Outline each Plasmodium vivax-infected red blood cell.
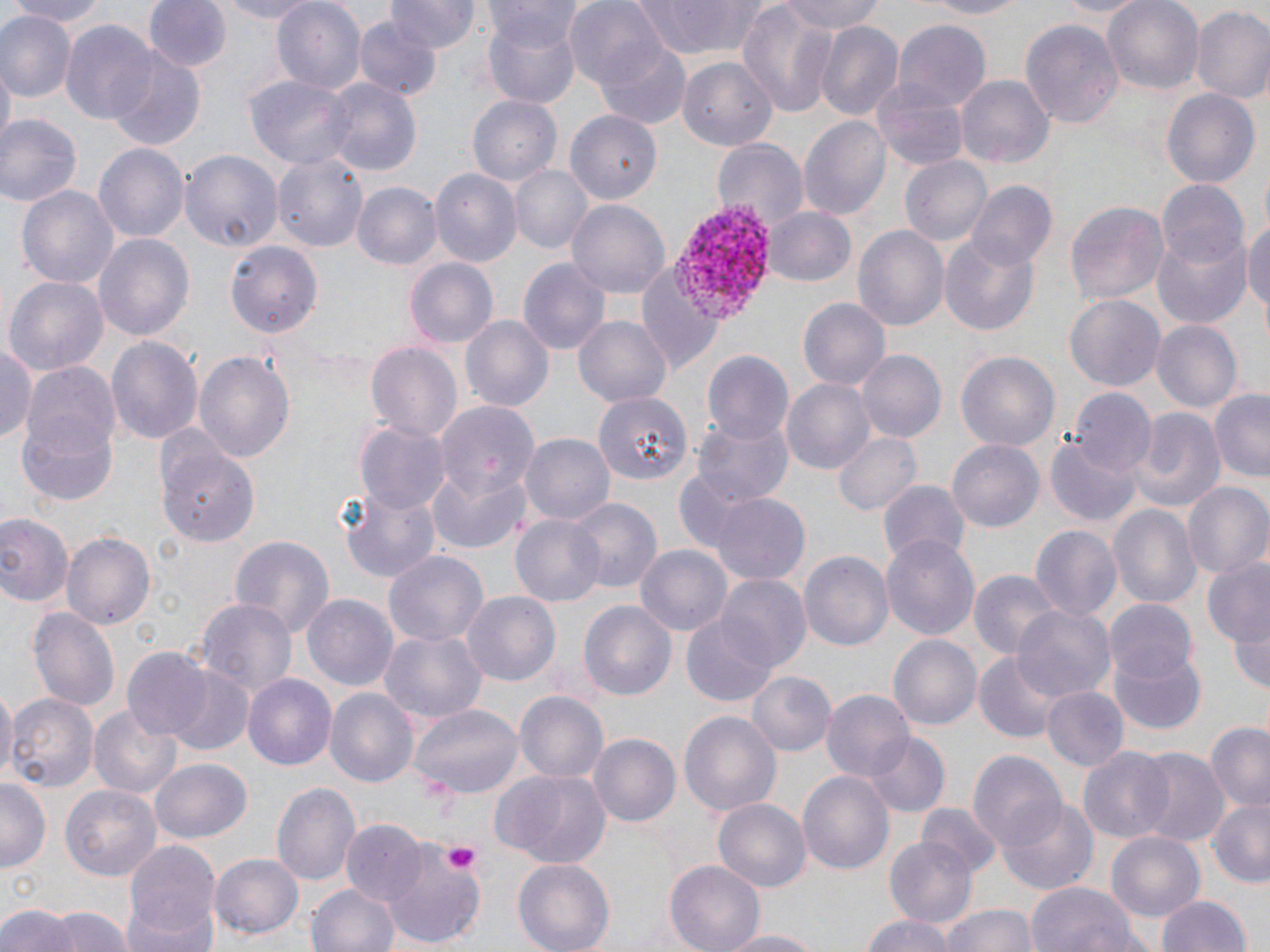
Approximate bounding boxes as named x1/y1/x2/y2 corners in pixels.
Plasmodium vivax-infected red blood cells: (x1=672, y1=202, x2=779, y2=319).

Platelet locations: (x1=445, y1=842, x2=480, y2=873). Uninfected red blood cell locations: (x1=1, y1=0, x2=112, y2=25), (x1=143, y1=0, x2=228, y2=73), (x1=204, y1=0, x2=325, y2=23), (x1=387, y1=0, x2=480, y2=54), (x1=565, y1=0, x2=667, y2=90), (x1=915, y1=0, x2=1032, y2=19), (x1=1053, y1=0, x2=1151, y2=18), (x1=1101, y1=0, x2=1203, y2=94), (x1=484, y1=1, x2=583, y2=53), (x1=626, y1=1, x2=780, y2=59), (x1=779, y1=1, x2=885, y2=38), (x1=271, y1=2, x2=364, y2=94), (x1=737, y1=2, x2=836, y2=119), (x1=1188, y1=3, x2=1270, y2=104), (x1=0, y1=12, x2=74, y2=103), (x1=482, y1=13, x2=582, y2=108), (x1=356, y1=15, x2=440, y2=100), (x1=1021, y1=18, x2=1123, y2=133), (x1=1173, y1=18, x2=1266, y2=172), (x1=815, y1=19, x2=905, y2=118), (x1=60, y1=20, x2=160, y2=126), (x1=894, y1=22, x2=990, y2=108), (x1=595, y1=40, x2=691, y2=129), (x1=106, y1=50, x2=206, y2=148), (x1=678, y1=56, x2=779, y2=151), (x1=871, y1=74, x2=971, y2=171), (x1=957, y1=75, x2=1052, y2=170), (x1=245, y1=76, x2=355, y2=168), (x1=322, y1=78, x2=421, y2=174), (x1=1162, y1=87, x2=1260, y2=192), (x1=468, y1=95, x2=562, y2=187), (x1=566, y1=110, x2=660, y2=204), (x1=1, y1=114, x2=81, y2=206), (x1=800, y1=116, x2=892, y2=223), (x1=711, y1=137, x2=808, y2=229), (x1=95, y1=143, x2=188, y2=242), (x1=180, y1=150, x2=284, y2=251), (x1=273, y1=151, x2=369, y2=256), (x1=900, y1=156, x2=992, y2=249), (x1=509, y1=166, x2=591, y2=255), (x1=430, y1=168, x2=520, y2=268), (x1=1155, y1=178, x2=1248, y2=270), (x1=354, y1=181, x2=440, y2=270), (x1=965, y1=182, x2=1057, y2=273), (x1=18, y1=184, x2=116, y2=292), (x1=566, y1=198, x2=670, y2=300), (x1=1067, y1=200, x2=1169, y2=307), (x1=763, y1=206, x2=856, y2=288), (x1=1244, y1=211, x2=1270, y2=325), (x1=852, y1=225, x2=948, y2=335), (x1=1150, y1=229, x2=1250, y2=329), (x1=95, y1=232, x2=195, y2=342), (x1=939, y1=236, x2=1040, y2=336), (x1=223, y1=240, x2=325, y2=341), (x1=635, y1=257, x2=723, y2=373), (x1=405, y1=258, x2=497, y2=348), (x1=518, y1=260, x2=610, y2=357), (x1=4, y1=276, x2=108, y2=378), (x1=1065, y1=295, x2=1164, y2=392), (x1=798, y1=297, x2=891, y2=389), (x1=575, y1=315, x2=673, y2=408), (x1=461, y1=316, x2=553, y2=410), (x1=1152, y1=320, x2=1241, y2=414), (x1=106, y1=335, x2=205, y2=451), (x1=365, y1=340, x2=463, y2=445), (x1=0, y1=341, x2=37, y2=447), (x1=856, y1=350, x2=945, y2=442), (x1=194, y1=351, x2=296, y2=467), (x1=702, y1=351, x2=792, y2=445), (x1=957, y1=352, x2=1059, y2=453), (x1=17, y1=359, x2=121, y2=478), (x1=783, y1=377, x2=877, y2=475), (x1=1071, y1=387, x2=1157, y2=476), (x1=1210, y1=388, x2=1270, y2=482), (x1=593, y1=391, x2=690, y2=485), (x1=431, y1=404, x2=538, y2=518), (x1=1125, y1=408, x2=1223, y2=515), (x1=692, y1=417, x2=793, y2=507), (x1=356, y1=422, x2=447, y2=511), (x1=835, y1=429, x2=921, y2=517), (x1=520, y1=432, x2=614, y2=526), (x1=155, y1=436, x2=263, y2=545), (x1=1046, y1=436, x2=1142, y2=527), (x1=947, y1=440, x2=1043, y2=534), (x1=428, y1=470, x2=531, y2=553), (x1=879, y1=480, x2=968, y2=569), (x1=337, y1=482, x2=443, y2=586), (x1=1183, y1=484, x2=1269, y2=581), (x1=706, y1=491, x2=811, y2=584), (x1=564, y1=497, x2=660, y2=593), (x1=1108, y1=505, x2=1200, y2=607), (x1=0, y1=513, x2=72, y2=608), (x1=512, y1=514, x2=605, y2=609), (x1=1029, y1=524, x2=1121, y2=622), (x1=63, y1=531, x2=155, y2=630), (x1=881, y1=531, x2=979, y2=640), (x1=228, y1=535, x2=336, y2=639), (x1=636, y1=546, x2=730, y2=635), (x1=384, y1=549, x2=489, y2=649), (x1=799, y1=551, x2=894, y2=650), (x1=1203, y1=553, x2=1270, y2=660), (x1=967, y1=569, x2=1059, y2=661), (x1=716, y1=575, x2=809, y2=673), (x1=460, y1=591, x2=561, y2=686), (x1=303, y1=593, x2=401, y2=691), (x1=193, y1=596, x2=296, y2=701), (x1=578, y1=598, x2=676, y2=698), (x1=1107, y1=598, x2=1200, y2=686), (x1=1012, y1=604, x2=1113, y2=702), (x1=1227, y1=604, x2=1270, y2=698), (x1=29, y1=608, x2=119, y2=714), (x1=677, y1=612, x2=786, y2=707), (x1=379, y1=628, x2=487, y2=729), (x1=888, y1=636, x2=980, y2=728), (x1=1111, y1=645, x2=1208, y2=733), (x1=121, y1=649, x2=213, y2=740), (x1=974, y1=652, x2=1058, y2=741), (x1=165, y1=667, x2=256, y2=757), (x1=749, y1=672, x2=834, y2=756), (x1=244, y1=674, x2=336, y2=772), (x1=1041, y1=686, x2=1129, y2=772), (x1=325, y1=688, x2=418, y2=790), (x1=0, y1=690, x2=16, y2=783), (x1=822, y1=690, x2=915, y2=784), (x1=515, y1=691, x2=608, y2=788), (x1=7, y1=694, x2=98, y2=793), (x1=411, y1=703, x2=524, y2=801), (x1=89, y1=704, x2=182, y2=799), (x1=678, y1=710, x2=782, y2=818), (x1=1204, y1=723, x2=1270, y2=813), (x1=866, y1=732, x2=950, y2=818), (x1=589, y1=735, x2=679, y2=825), (x1=1078, y1=747, x2=1175, y2=843), (x1=1135, y1=748, x2=1228, y2=847), (x1=968, y1=751, x2=1065, y2=853), (x1=150, y1=760, x2=251, y2=845), (x1=491, y1=767, x2=610, y2=868), (x1=798, y1=770, x2=894, y2=877), (x1=0, y1=780, x2=49, y2=874), (x1=273, y1=782, x2=362, y2=888), (x1=59, y1=784, x2=161, y2=881), (x1=1206, y1=796, x2=1270, y2=887), (x1=712, y1=799, x2=811, y2=893), (x1=999, y1=799, x2=1098, y2=893), (x1=918, y1=803, x2=1002, y2=880), (x1=342, y1=821, x2=429, y2=909), (x1=1105, y1=832, x2=1206, y2=924), (x1=884, y1=836, x2=976, y2=928), (x1=122, y1=838, x2=221, y2=946), (x1=378, y1=839, x2=486, y2=947), (x1=211, y1=852, x2=304, y2=940), (x1=513, y1=857, x2=615, y2=952), (x1=664, y1=860, x2=764, y2=952), (x1=309, y1=882, x2=400, y2=952), (x1=1027, y1=882, x2=1141, y2=952), (x1=1155, y1=894, x2=1252, y2=952), (x1=0, y1=903, x2=78, y2=952), (x1=123, y1=903, x2=214, y2=952), (x1=937, y1=903, x2=1043, y2=952), (x1=51, y1=905, x2=130, y2=952), (x1=861, y1=914, x2=955, y2=952), (x1=712, y1=928, x2=829, y2=951). Slide-level diagnosis: Plasmodium vivax. Image is 1270×952 pixels. Optical microscopy. One field of a larger specimen. May-Grünwald-Giemsa stain. Thin blood film. Captured at 1000x magnification.